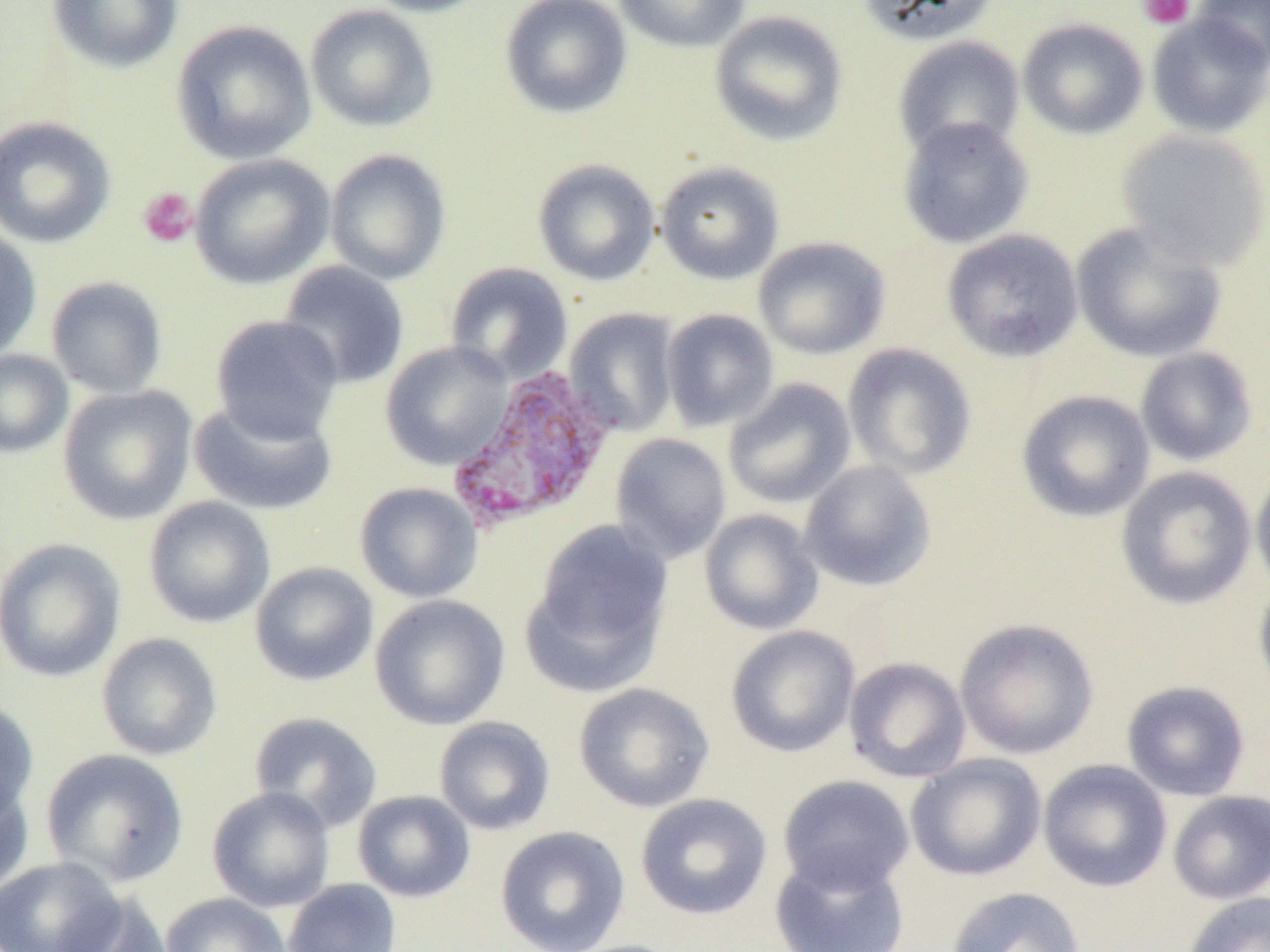 Approximate bounding boxes as named x1/y1/x2/y2 corners in pixels. Plasmodium vivax-infected red blood cell locations: (x1=446, y1=363, x2=616, y2=532). Platelet locations: (x1=1137, y1=0, x2=1195, y2=29), (x1=138, y1=187, x2=198, y2=247). Uninfected red blood cell locations: (x1=47, y1=0, x2=183, y2=73), (x1=360, y1=0, x2=494, y2=17), (x1=500, y1=0, x2=633, y2=119), (x1=613, y1=0, x2=751, y2=53), (x1=857, y1=0, x2=999, y2=45), (x1=1193, y1=1, x2=1270, y2=72), (x1=305, y1=3, x2=440, y2=132), (x1=709, y1=10, x2=849, y2=146), (x1=1146, y1=14, x2=1270, y2=139), (x1=1017, y1=18, x2=1149, y2=140), (x1=171, y1=20, x2=316, y2=164), (x1=893, y1=35, x2=1026, y2=159), (x1=0, y1=116, x2=116, y2=248), (x1=897, y1=116, x2=1034, y2=249), (x1=1116, y1=129, x2=1270, y2=271), (x1=325, y1=149, x2=451, y2=285), (x1=190, y1=154, x2=334, y2=289), (x1=532, y1=159, x2=660, y2=286), (x1=655, y1=161, x2=785, y2=285), (x1=1071, y1=220, x2=1227, y2=362), (x1=0, y1=228, x2=42, y2=364), (x1=942, y1=229, x2=1084, y2=363), (x1=753, y1=236, x2=891, y2=360), (x1=278, y1=261, x2=410, y2=390), (x1=445, y1=262, x2=573, y2=383), (x1=46, y1=276, x2=168, y2=399), (x1=564, y1=308, x2=679, y2=437), (x1=661, y1=309, x2=779, y2=432), (x1=210, y1=315, x2=344, y2=444), (x1=381, y1=341, x2=514, y2=471), (x1=843, y1=343, x2=978, y2=481), (x1=1135, y1=347, x2=1258, y2=466), (x1=0, y1=349, x2=73, y2=457), (x1=722, y1=378, x2=857, y2=511), (x1=58, y1=385, x2=197, y2=525), (x1=1016, y1=390, x2=1155, y2=522), (x1=189, y1=397, x2=337, y2=515), (x1=609, y1=432, x2=731, y2=564), (x1=799, y1=460, x2=937, y2=592), (x1=1251, y1=461, x2=1270, y2=600), (x1=1116, y1=466, x2=1257, y2=610), (x1=354, y1=482, x2=483, y2=603), (x1=143, y1=496, x2=275, y2=628), (x1=699, y1=509, x2=824, y2=635), (x1=525, y1=520, x2=673, y2=687), (x1=0, y1=538, x2=126, y2=682), (x1=250, y1=562, x2=379, y2=686), (x1=1254, y1=576, x2=1270, y2=704), (x1=370, y1=594, x2=510, y2=730), (x1=954, y1=618, x2=1100, y2=760), (x1=726, y1=625, x2=860, y2=758), (x1=96, y1=632, x2=223, y2=761), (x1=844, y1=656, x2=971, y2=783), (x1=1122, y1=681, x2=1251, y2=801), (x1=573, y1=683, x2=714, y2=813), (x1=0, y1=700, x2=38, y2=827), (x1=249, y1=711, x2=382, y2=832), (x1=434, y1=716, x2=556, y2=835), (x1=41, y1=749, x2=189, y2=887), (x1=906, y1=754, x2=1046, y2=881), (x1=1038, y1=759, x2=1172, y2=892), (x1=778, y1=775, x2=914, y2=895), (x1=0, y1=782, x2=34, y2=897), (x1=207, y1=786, x2=335, y2=912), (x1=352, y1=790, x2=475, y2=902), (x1=1167, y1=790, x2=1270, y2=905), (x1=635, y1=793, x2=772, y2=920), (x1=495, y1=826, x2=631, y2=952), (x1=770, y1=853, x2=911, y2=952), (x1=0, y1=857, x2=126, y2=952), (x1=283, y1=878, x2=402, y2=952), (x1=946, y1=886, x2=1085, y2=952), (x1=1182, y1=892, x2=1270, y2=952), (x1=161, y1=893, x2=293, y2=952), (x1=55, y1=894, x2=174, y2=952). Slide-level diagnosis: Plasmodium vivax. 1000x magnification. Image is 1270×952 pixels. Optical microscopy. One field of a larger specimen. Thin blood film.